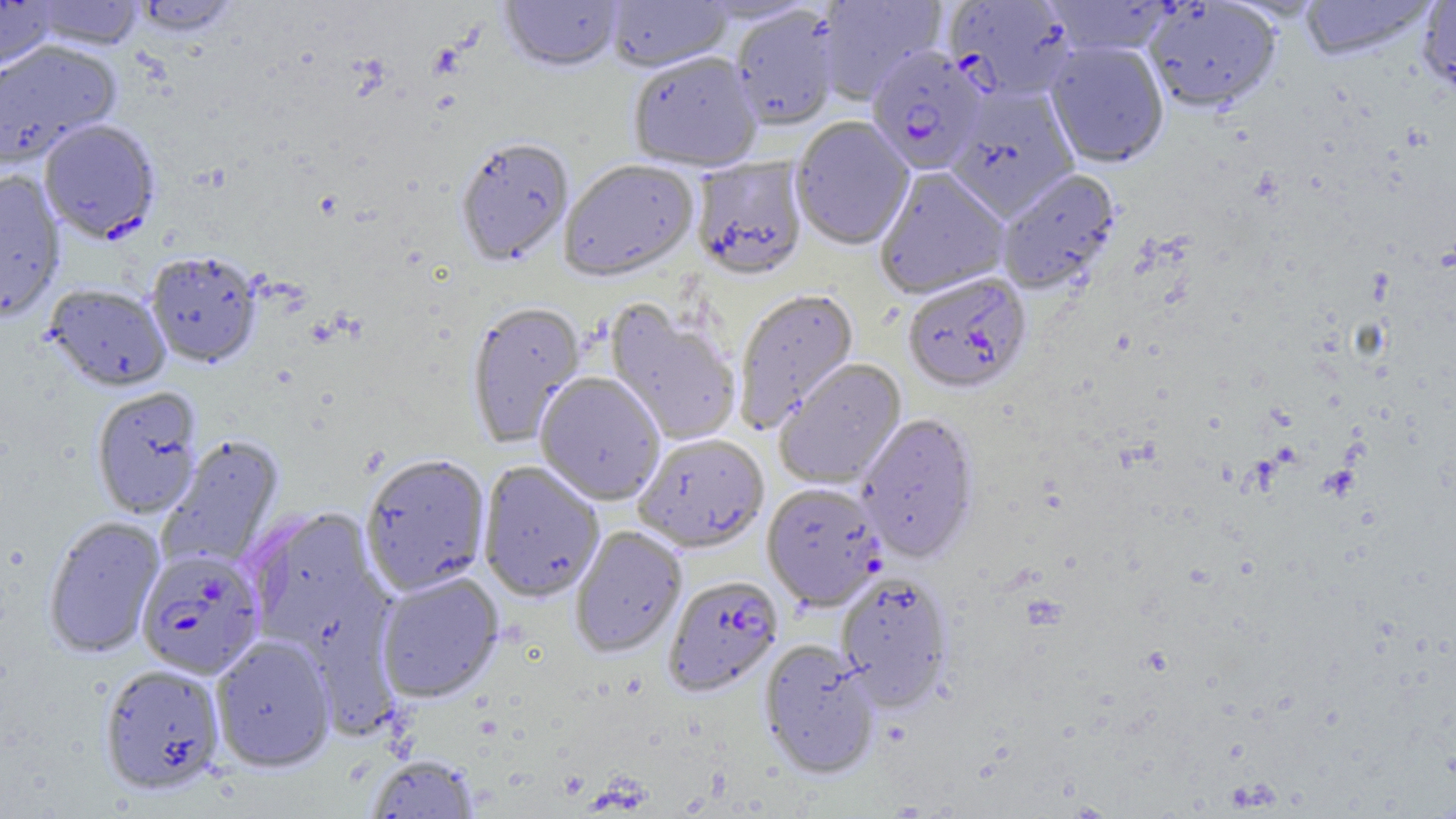
plasmodium_falciparum_infected_red_blood_cell_locations: 'approximate bounding boxes as named x1/y1/x2/y2 corners in pixels: (x1=944, y1=1, x2=1077, y2=102), (x1=865, y1=47, x2=987, y2=176), (x1=39, y1=120, x2=161, y2=245), (x1=903, y1=273, x2=1032, y2=396), (x1=137, y1=550, x2=264, y2=679), (x1=664, y1=576, x2=782, y2=696)'
slide_level_diagnosis: Plasmodium falciparum
uninfected_red_blood_cell_locations: 'approximate bounding boxes as named x1/y1/x2/y2 corners in pixels: (x1=500, y1=0, x2=623, y2=75), (x1=816, y1=0, x2=946, y2=104), (x1=1043, y1=0, x2=1177, y2=56), (x1=1299, y1=0, x2=1437, y2=62), (x1=1418, y1=0, x2=1456, y2=98), (x1=0, y1=1, x2=59, y2=74), (x1=27, y1=1, x2=146, y2=51), (x1=129, y1=1, x2=240, y2=37), (x1=604, y1=1, x2=733, y2=73), (x1=1144, y1=1, x2=1282, y2=113), (x1=730, y1=6, x2=841, y2=132), (x1=0, y1=40, x2=122, y2=168), (x1=1045, y1=41, x2=1169, y2=168), (x1=628, y1=53, x2=762, y2=174), (x1=946, y1=86, x2=1080, y2=221), (x1=791, y1=117, x2=914, y2=252), (x1=456, y1=140, x2=574, y2=268), (x1=692, y1=158, x2=809, y2=282), (x1=559, y1=162, x2=700, y2=283), (x1=874, y1=167, x2=1010, y2=300), (x1=997, y1=169, x2=1120, y2=295), (x1=0, y1=171, x2=66, y2=322), (x1=146, y1=252, x2=261, y2=369), (x1=45, y1=286, x2=171, y2=393), (x1=733, y1=289, x2=859, y2=432), (x1=466, y1=303, x2=586, y2=448), (x1=604, y1=303, x2=742, y2=446), (x1=775, y1=359, x2=906, y2=489), (x1=535, y1=373, x2=665, y2=507), (x1=91, y1=387, x2=203, y2=519), (x1=856, y1=414, x2=979, y2=564), (x1=633, y1=435, x2=769, y2=554), (x1=160, y1=436, x2=284, y2=572), (x1=360, y1=454, x2=492, y2=596), (x1=477, y1=462, x2=605, y2=603), (x1=762, y1=484, x2=886, y2=612), (x1=247, y1=507, x2=385, y2=650), (x1=44, y1=516, x2=165, y2=659), (x1=570, y1=526, x2=686, y2=659), (x1=836, y1=572, x2=953, y2=712), (x1=375, y1=573, x2=504, y2=704), (x1=210, y1=637, x2=335, y2=773), (x1=759, y1=641, x2=879, y2=780), (x1=99, y1=663, x2=226, y2=796), (x1=365, y1=754, x2=480, y2=818)'
preparation: thin blood smear
magnification: 1000x
field_of_view: one of a larger specimen
modality: optical microscopy
image_size: 1456×819 pixels